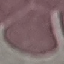

{
  "result": "negative for malaria parasites",
  "capture": "smartphone camera at the microscope eyepiece",
  "preparation": "thin smear",
  "stain": "Giemsa",
  "image_type": "cell patch, automatically extracted from a larger field of view and resized to 64 × 64 pixels"
}